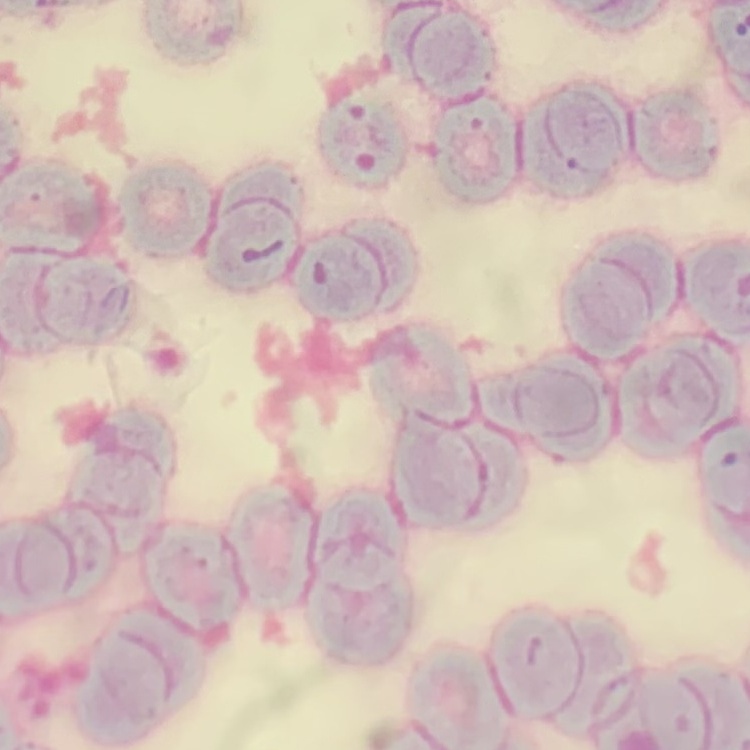
Summary:
  - Red blood cell morphology: rouleaux formation
  - Image type: one tile cut from a larger photomicrograph
  - Preparation: thin peripheral smear
  - Stain: Field's or Giemsa